Give the extent of the Plasmodium falciparum parasites you find, grouped by life-cycle stage — ring form, trophozoite, schizont, or gametocyte.
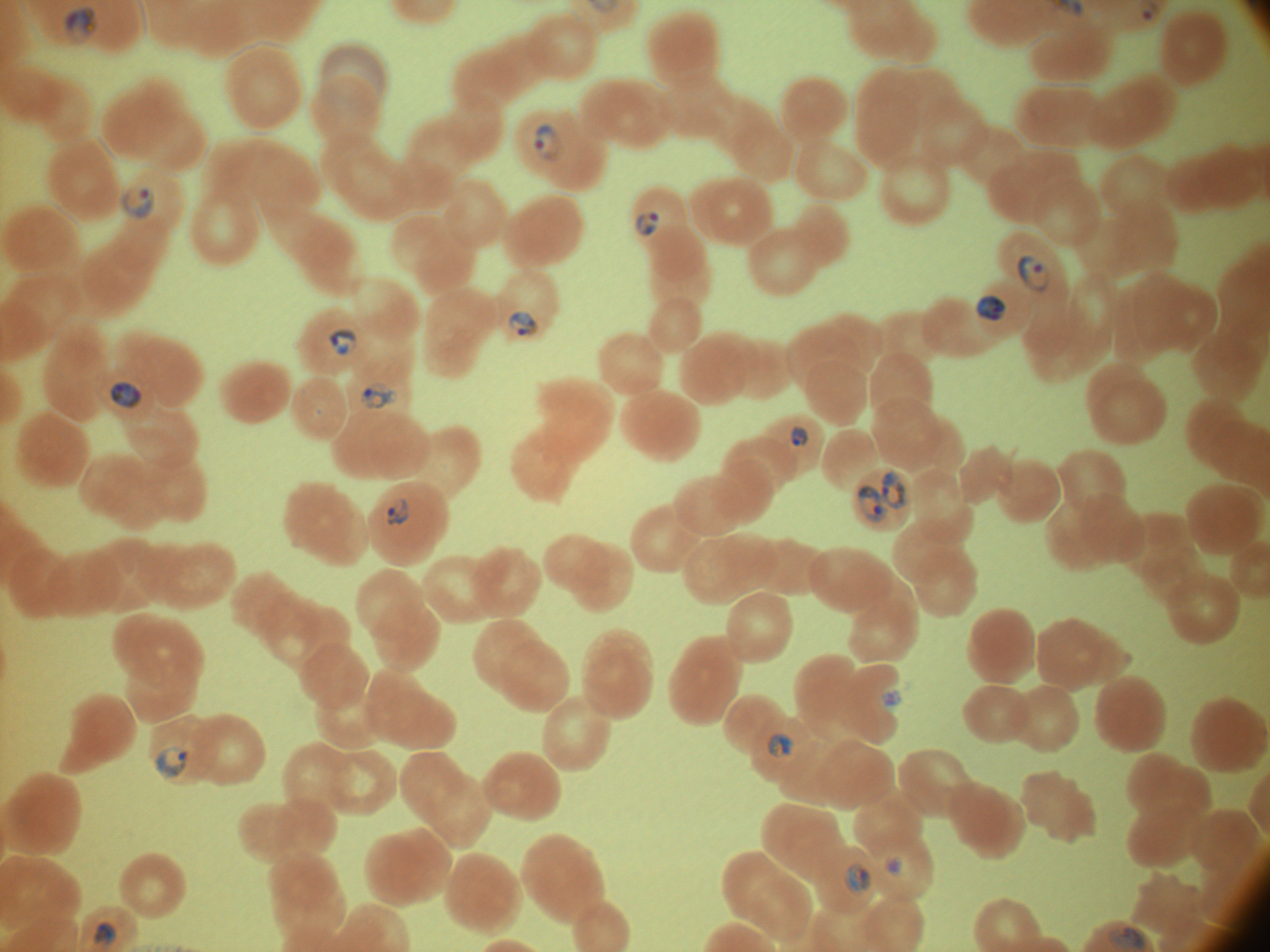
Approximate bounding boxes as named x1/y1/x2/y2 corners in pixels, from the source annotation, which is not necessarily exhaustive.
Ring forms: (x1=63, y1=6, x2=98, y2=48), (x1=1142, y1=9, x2=1152, y2=22), (x1=533, y1=122, x2=564, y2=162), (x1=121, y1=185, x2=156, y2=222), (x1=635, y1=211, x2=661, y2=236), (x1=1018, y1=253, x2=1050, y2=293), (x1=977, y1=294, x2=1007, y2=321), (x1=507, y1=311, x2=537, y2=336), (x1=328, y1=328, x2=359, y2=356), (x1=108, y1=380, x2=145, y2=411), (x1=361, y1=381, x2=398, y2=409), (x1=790, y1=426, x2=808, y2=448), (x1=880, y1=471, x2=906, y2=510), (x1=858, y1=484, x2=887, y2=523), (x1=384, y1=498, x2=410, y2=526), (x1=882, y1=691, x2=902, y2=708), (x1=767, y1=733, x2=794, y2=758), (x1=156, y1=745, x2=188, y2=779), (x1=883, y1=855, x2=903, y2=876), (x1=844, y1=863, x2=871, y2=895), (x1=92, y1=921, x2=118, y2=947).

{
  "species": "Plasmodium falciparum",
  "stain": "Giemsa",
  "image_size": "1270×952 pixels",
  "preparation": "thin blood smear",
  "magnification": "100x",
  "microscope": "Leica DM2000 with built-in camera",
  "field_of_view": "single"
}